Assess the morphology of the erythrocytes.
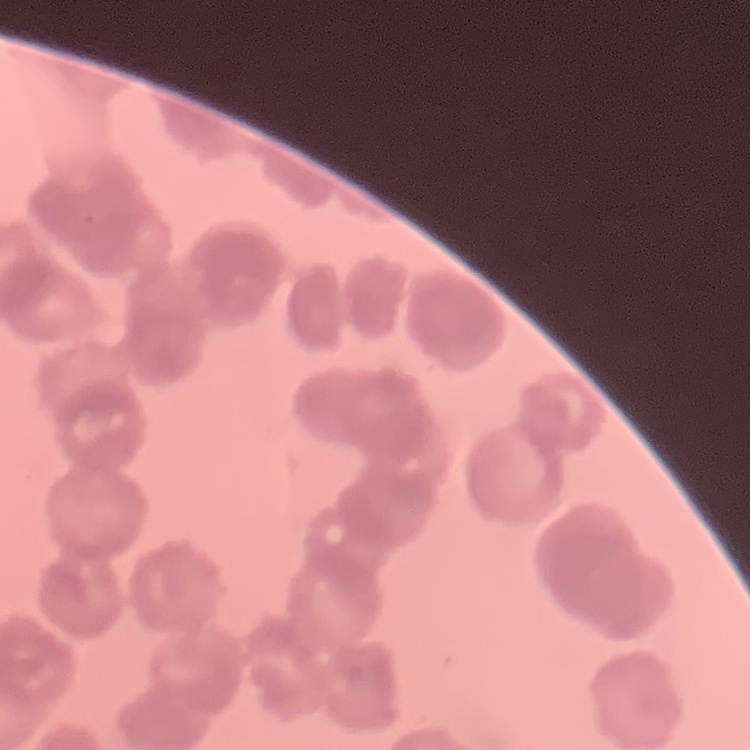

Rouleaux formation.

image_type: square crop of a larger photomicrograph
preparation: thin peripheral smear
stain: Field's or Giemsa